Name the cell type shown.
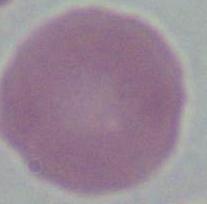
An erythrocyte.

magnification: 1000x
modality: micrograph